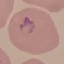

Summary:
  - Malaria status: parasitized
  - Capture: smartphone through the microscope eyepiece
  - Stain: Giemsa
  - Image type: automatically extracted cell patch, resized to 64 × 64 pixels
  - Preparation: thin smear